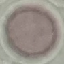

Result: no malaria parasites detected. Cell patch, automatically extracted from a larger field of view and resized to 64 × 64 pixels. Acquired by smartphone through the microscope eyepiece. Thin blood film. Giemsa-stained preparation.